Outline each Plasmodium malariae-infected red blood cell.
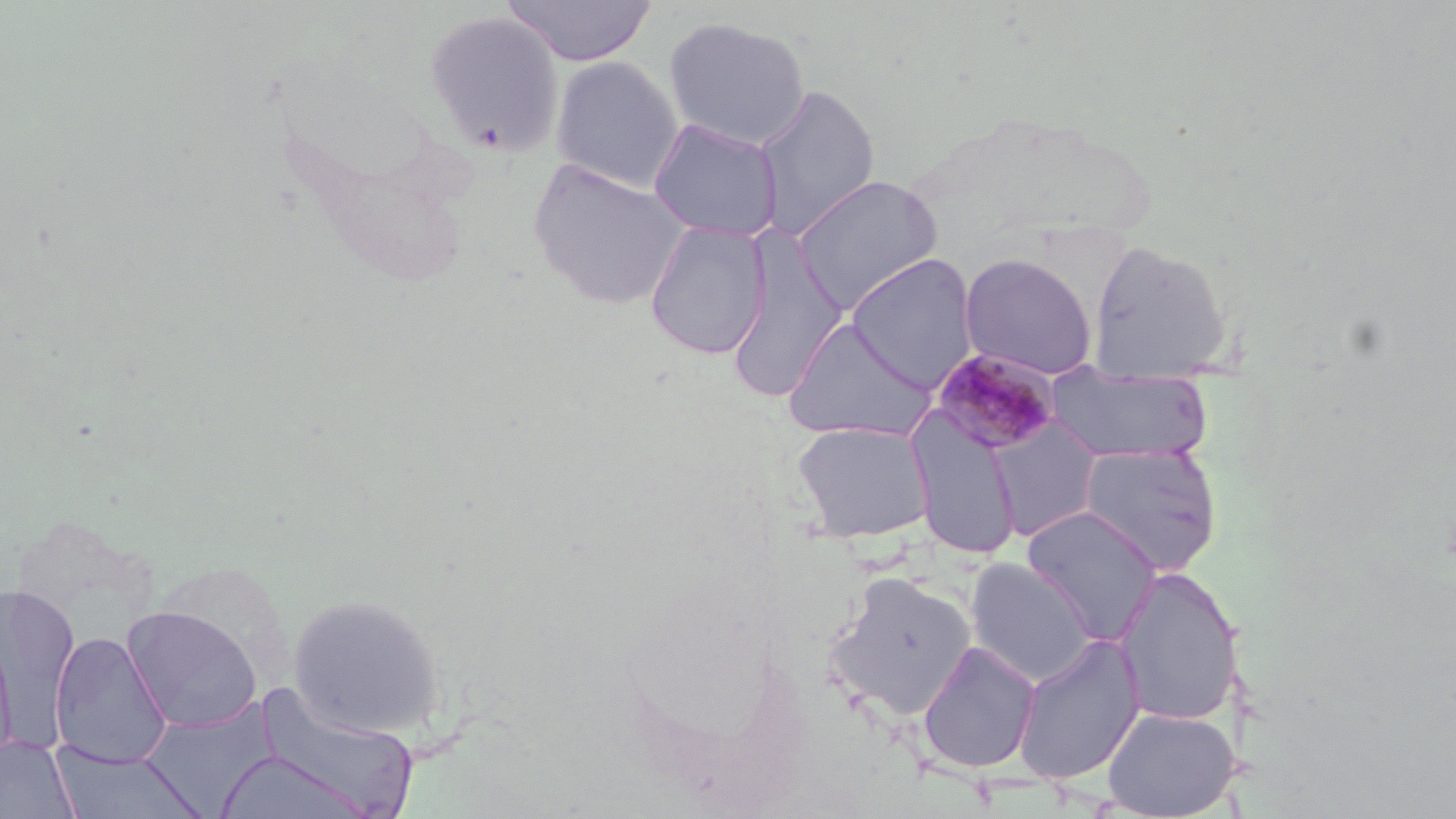
Approximate bounding boxes as (x1, y1, x2, y2) in pixels.
Plasmodium malariae-infected red blood cells: (930, 347, 1063, 455).

{
  "slide_level_diagnosis": "Plasmodium malariae",
  "uninfected_red_blood_cell_locations": "approximate bounding boxes as (x1, y1, x2, y2) in pixels: (502, 1, 658, 66), (424, 10, 566, 155), (663, 15, 811, 150), (549, 54, 684, 193), (754, 83, 881, 241), (648, 118, 783, 241), (528, 157, 691, 311), (790, 174, 944, 314), (644, 220, 771, 360), (1085, 239, 1235, 382), (726, 240, 849, 403), (959, 252, 1098, 380), (845, 253, 979, 392), (783, 316, 937, 442), (1046, 366, 1213, 465), (907, 406, 1023, 560), (986, 417, 1105, 542), (792, 420, 935, 543), (1075, 442, 1223, 577), (1021, 505, 1162, 644), (965, 558, 1096, 687), (1114, 565, 1244, 727), (827, 571, 976, 721), (1, 585, 79, 736), (288, 592, 448, 738), (122, 605, 263, 733), (52, 632, 172, 767), (1011, 632, 1146, 786), (0, 633, 18, 764), (916, 640, 1041, 774), (252, 685, 421, 819), (140, 701, 280, 813), (1101, 705, 1239, 818), (0, 736, 79, 819), (49, 744, 205, 818), (214, 749, 372, 819)",
  "magnification": "1000x",
  "image_size": "1456×819 pixels",
  "field_of_view": "single",
  "stain": "May-Grünwald-Giemsa",
  "preparation": "thin blood smear",
  "modality": "light microscopy"
}